Describe the morphology of the red blood cells.
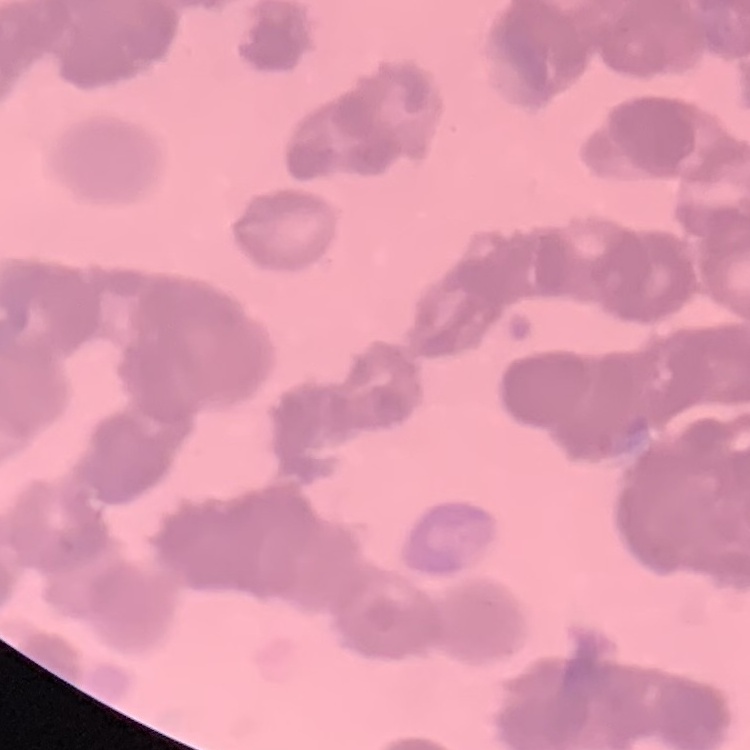
They show rouleaux formation.

Summary:
  - Image type: square crop of a larger photomicrograph
  - Stain: Field's or Giemsa
  - Preparation: thin blood smear